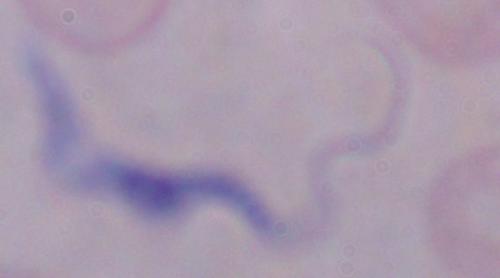
modality = micrograph
identification = trypanosome
magnification = 1000x